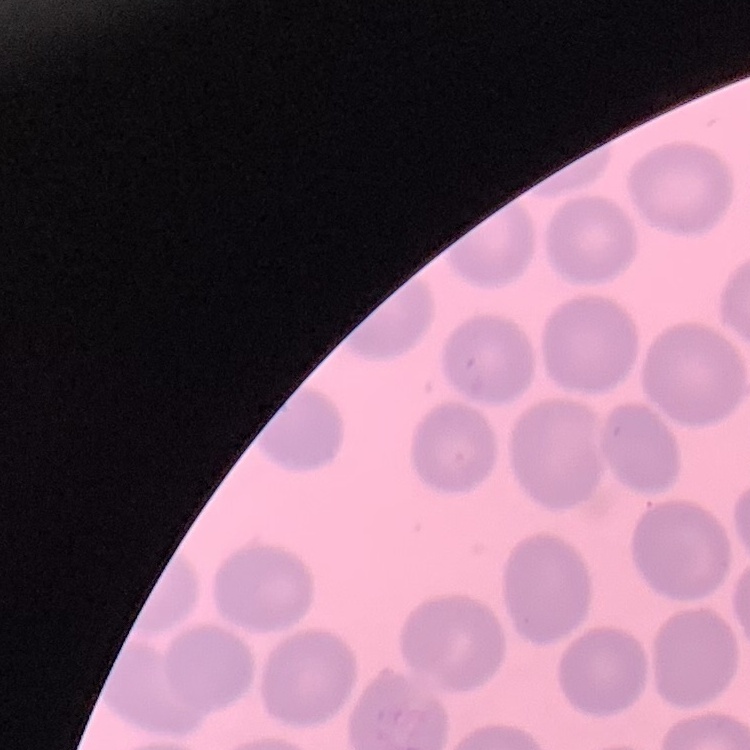

Summary:
  - Erythrocyte morphology: no rouleaux formation
  - Preparation: thin blood smear
  - Image type: square crop of a larger photomicrograph
  - Stain: Field's or Giemsa